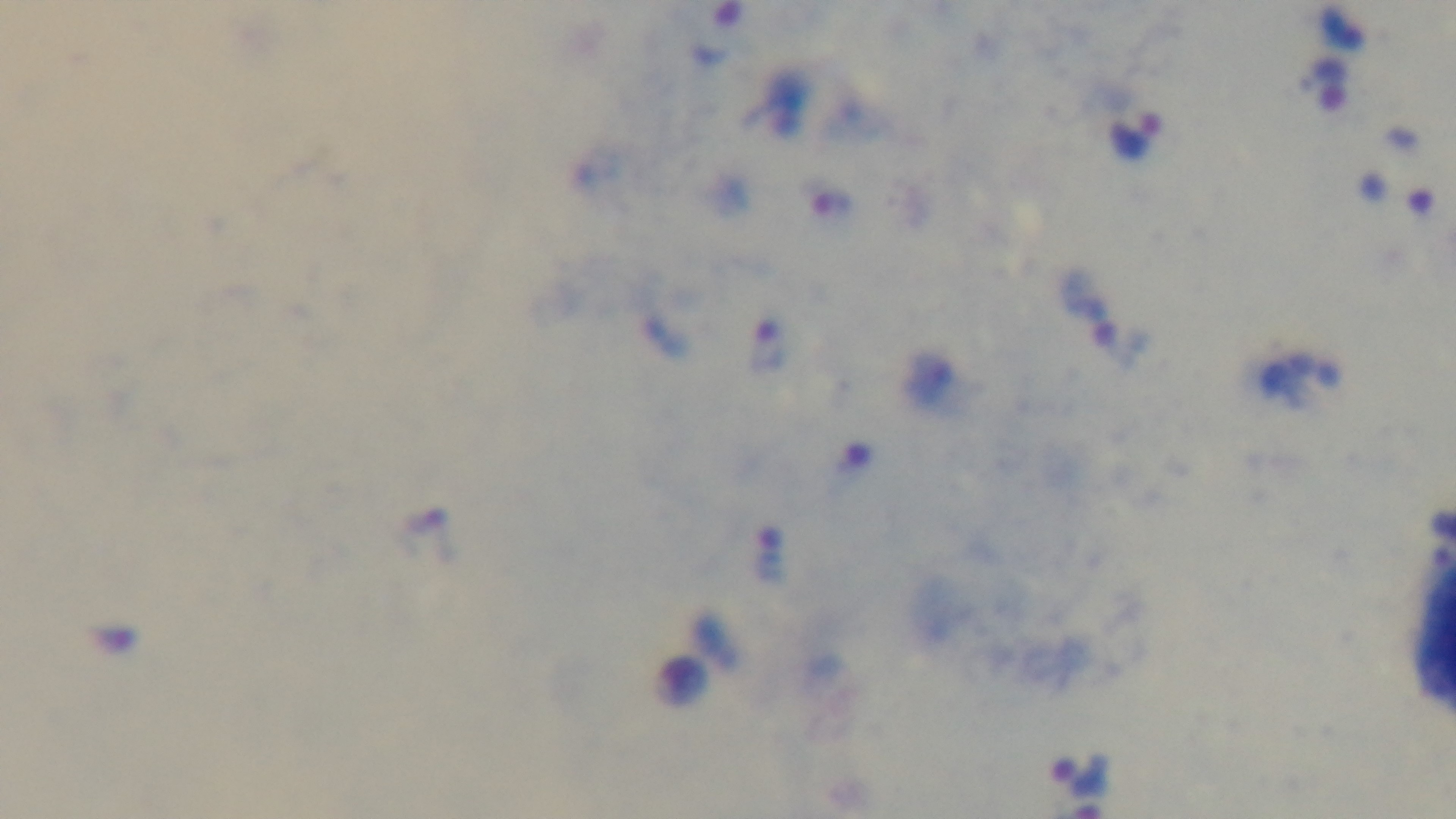
stain: Giemsa
field_of_view: one from the slide
objective: 100x oil immersion
modality: light microscopy
capture: mounted 4K digital camera
malaria_status: positive
preparation: thick